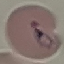

result = malaria parasites identified
preparation = thin blood smear
capture = smartphone camera at the microscope eyepiece
image type = cell patch, automatically extracted from a larger field of view and resized to 64 × 64 pixels
stain = Giemsa